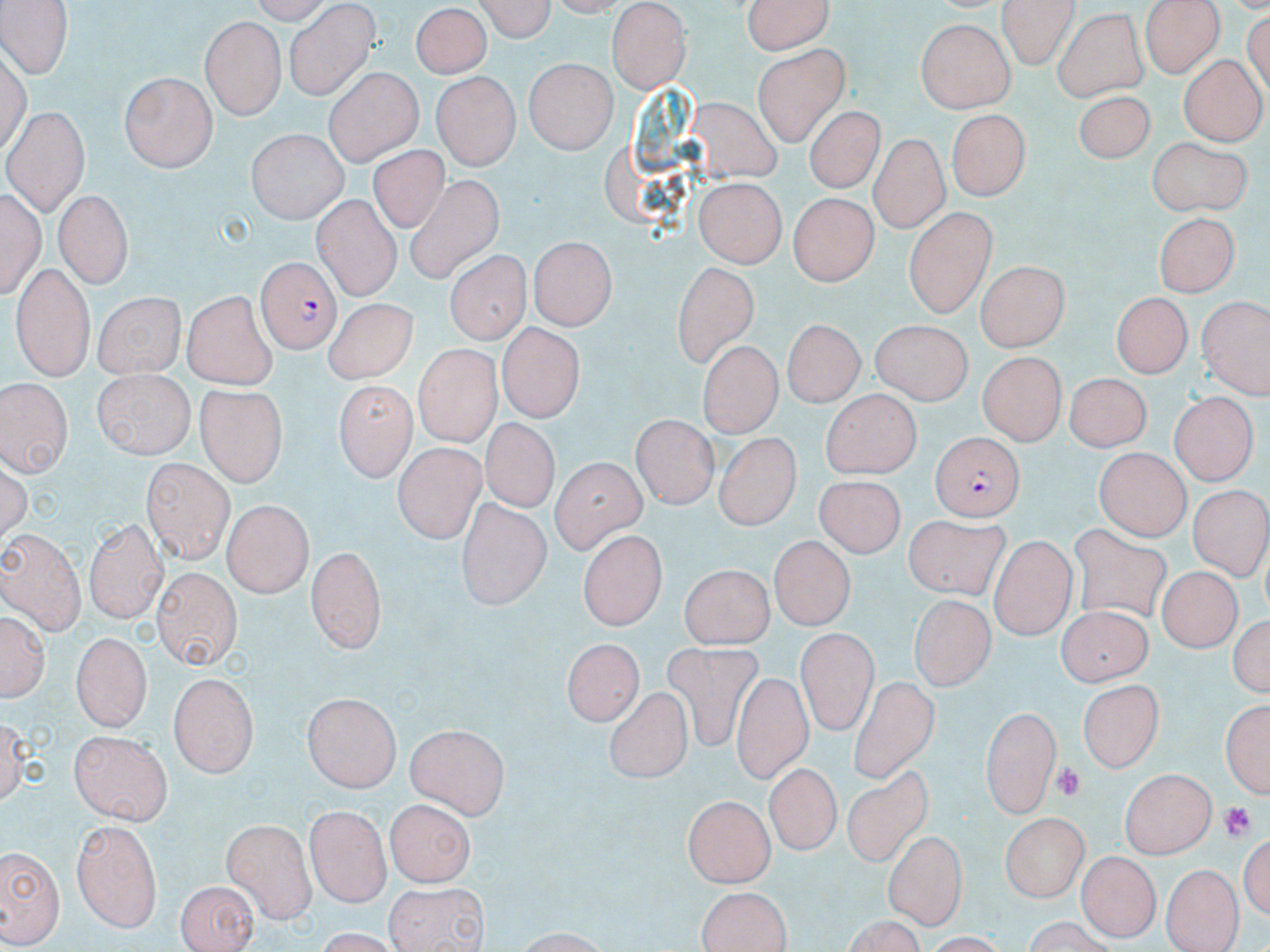
slide_level_diagnosis: Plasmodium falciparum
uninfected_red_blood_cell_locations: 'approximate bounding boxes as (x1, y1, x2, y2) in pixels: (0, 0, 71, 81), (470, 0, 557, 42), (741, 0, 837, 56), (995, 0, 1077, 67), (607, 3, 693, 92), (285, 4, 379, 97), (410, 4, 489, 80), (1140, 5, 1222, 80), (1052, 10, 1149, 100), (426, 15, 506, 153), (202, 16, 285, 119), (916, 23, 1012, 114), (141, 36, 273, 154), (753, 43, 851, 145), (524, 58, 617, 154), (1180, 59, 1264, 140), (324, 66, 424, 163), (431, 70, 525, 169), (119, 73, 215, 172), (1074, 93, 1162, 169), (702, 97, 781, 184), (9, 104, 88, 214), (803, 107, 884, 196), (946, 111, 1029, 203), (244, 129, 349, 222), (867, 135, 946, 233), (1144, 135, 1253, 214), (368, 145, 455, 233), (403, 173, 499, 286), (693, 180, 783, 269), (309, 187, 408, 301), (3, 189, 43, 306), (54, 191, 134, 287), (785, 194, 874, 287), (904, 211, 996, 318), (1151, 213, 1244, 293), (528, 237, 615, 329), (447, 252, 526, 347), (665, 262, 764, 378), (975, 262, 1066, 351), (10, 263, 92, 380), (181, 292, 277, 387), (93, 293, 188, 378), (1109, 294, 1191, 379), (1197, 297, 1267, 399), (320, 303, 427, 388), (783, 320, 863, 408), (868, 322, 971, 406), (497, 324, 584, 424), (696, 342, 778, 439), (413, 344, 499, 446), (976, 355, 1063, 444), (95, 369, 195, 457), (1063, 377, 1151, 459), (2, 379, 74, 476), (195, 382, 288, 483), (333, 383, 414, 479), (821, 390, 923, 480), (1171, 392, 1255, 488), (630, 416, 717, 508), (485, 421, 557, 508), (709, 426, 804, 536), (392, 443, 485, 542), (1094, 449, 1194, 538), (551, 459, 645, 553), (143, 460, 235, 560), (809, 472, 906, 561), (1184, 480, 1269, 584), (455, 496, 551, 610), (224, 501, 310, 596), (83, 517, 167, 620), (904, 518, 1014, 600), (1068, 521, 1170, 624), (0, 528, 85, 636), (579, 529, 664, 630), (769, 534, 852, 630), (989, 534, 1074, 638), (307, 546, 385, 653), (679, 564, 776, 644), (1157, 566, 1242, 652), (151, 567, 244, 667), (900, 592, 993, 686), (1055, 601, 1148, 685), (0, 610, 50, 703), (1232, 610, 1270, 699), (797, 630, 875, 735), (74, 632, 152, 732), (563, 637, 641, 725), (658, 641, 758, 754), (724, 668, 814, 785), (168, 673, 258, 777), (850, 674, 940, 787), (1078, 679, 1163, 774), (607, 688, 689, 784), (301, 692, 403, 794), (1220, 694, 1270, 800), (980, 704, 1061, 821), (5, 709, 37, 809), (407, 721, 509, 820), (69, 732, 173, 822), (766, 763, 838, 856), (1119, 766, 1215, 856), (840, 769, 936, 868), (683, 795, 775, 886), (386, 799, 478, 887), (304, 804, 392, 904), (998, 813, 1093, 899), (223, 818, 317, 921), (72, 820, 164, 931), (882, 829, 966, 930), (0, 844, 64, 946), (1076, 850, 1157, 941), (1162, 864, 1240, 951), (175, 876, 256, 952), (382, 878, 490, 952), (695, 888, 793, 952), (512, 927, 615, 951)'
modality: light microscopy
stain: May-Grünwald-Giemsa
magnification: 1000x
platelet_locations: 'approximate bounding boxes as (x1, y1, x2, y2) in pixels: (1054, 760, 1089, 802), (1219, 801, 1255, 844)'
preparation: thin blood smear
field_of_view: single
image_size: 1270×952 pixels
plasmodium_falciparum_infected_red_blood_cell_locations: 'approximate bounding boxes as (x1, y1, x2, y2) in pixels: (257, 258, 340, 351), (927, 430, 1028, 516)'